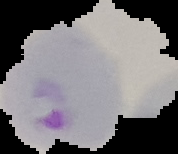

Image is 178×154 pixels. Result: Plasmodium parasites identified. The area outside the segmented cell region is set to black. From a thin blood film.